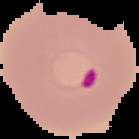 Image is 139×139 pixels. The area outside the segmented cell region is set to black. From a thin blood smear. Malaria status: parasitized.